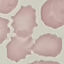

result = no malaria parasites seen
capture = smartphone camera at the microscope eyepiece
image type = automatically extracted cell patch, resized to 64 × 64 pixels
preparation = thin blood smear
stain = Giemsa